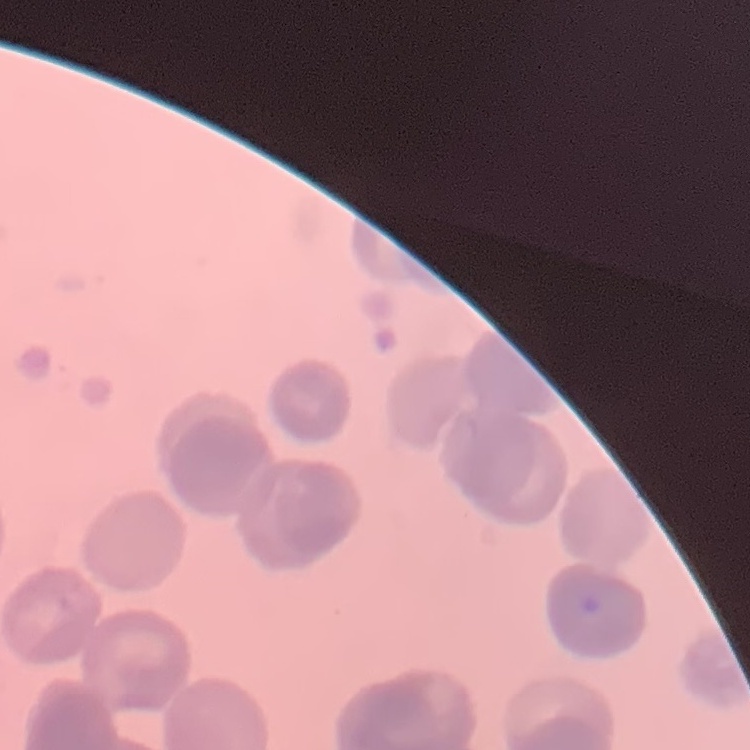
The erythrocytes exhibit rouleaux formation. Thin blood smear. One tile cut from a larger photomicrograph. Field's or Giemsa stain.